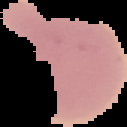 The area outside the segmented cell region is set to black. From a thin blood smear. Malaria status: uninfected. Image is 127×127 pixels.